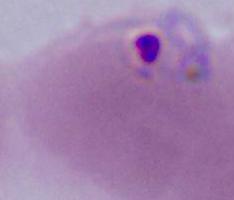
magnification: 400x or 1000x
identification: Plasmodium
modality: photomicrograph